Assess this cell for malaria.
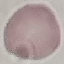

It is uninfected.

Automatically extracted cell patch, resized to 64 × 64 pixels. Photographed with a smartphone camera at the microscope eyepiece. Thin blood film. Giemsa stain.